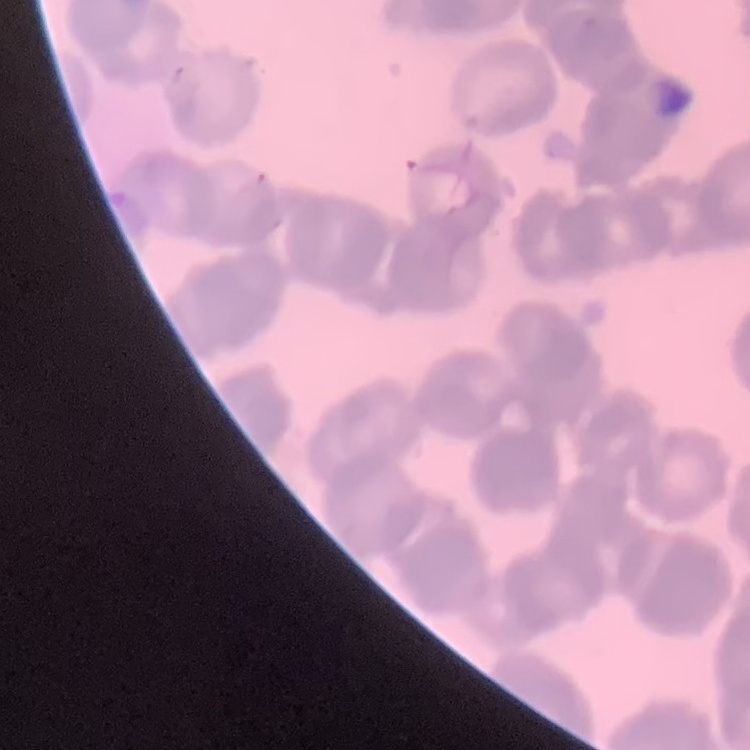
Summary:
  - Red blood cell morphology: rouleaux formation
  - Preparation: thin peripheral smear
  - Stain: Field's or Giemsa
  - Image type: one tile cut from a larger photomicrograph